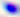
Summary:
  - Magnification: 400x
  - Identification: Toxoplasma gondii
  - Modality: micrograph